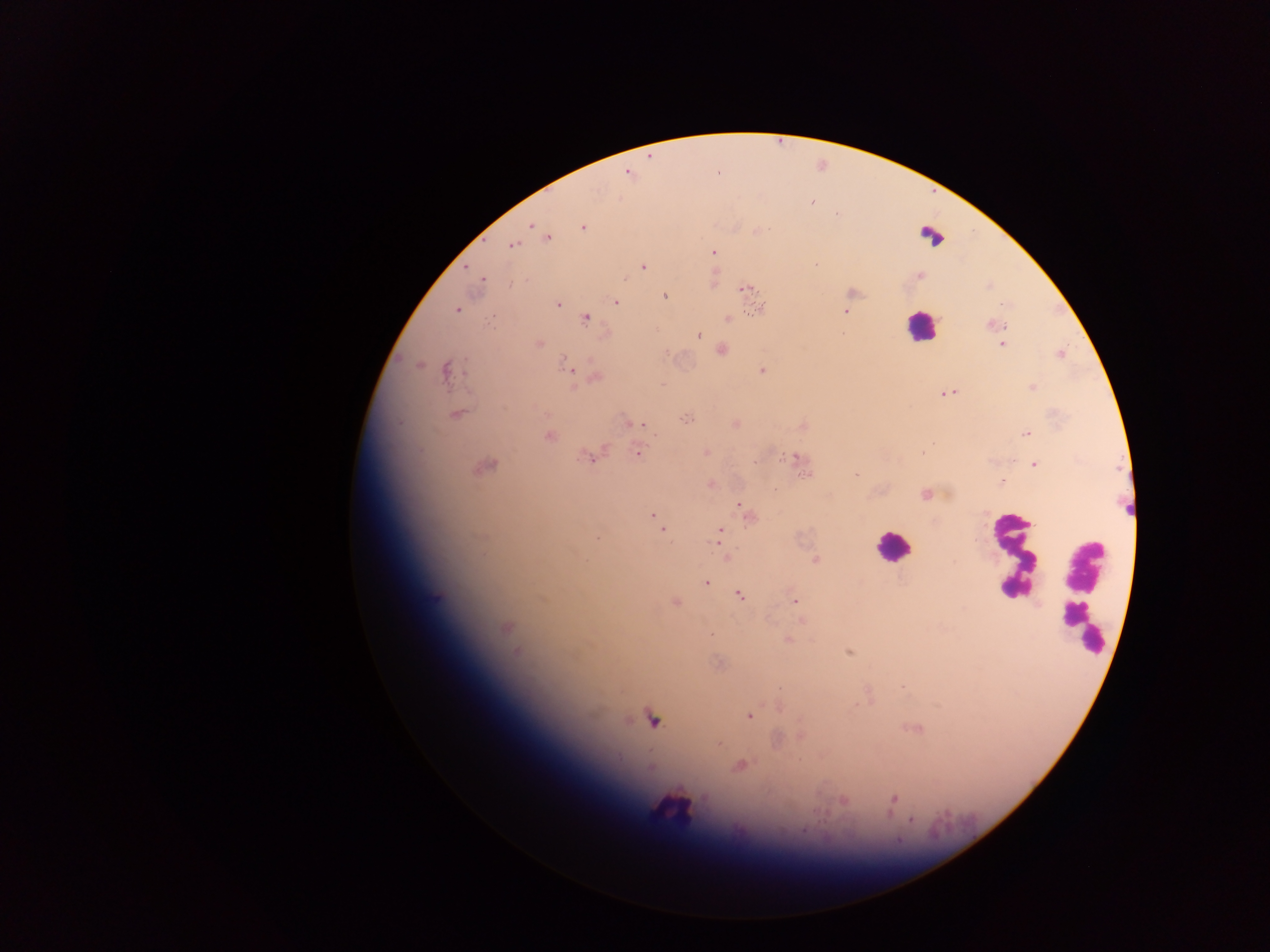
Approximate centers as x y in pixels.
Summary:
  - Leukocyte locations: 932 234; 920 327; 891 547; 1011 553; 1082 593; 674 806
  - Plasmodium parasite locations: 628 173; 811 203; 531 225; 583 227; 761 230; 547 238; 511 245; 713 253; 816 265; 643 267; 481 279; 745 288; 665 296; 616 302; 558 303; 1003 305; 760 308; 457 310; 844 311; 586 319; 727 319; 994 324; 698 336; 539 343; 1002 344; 721 351; 419 364; 567 366; 445 370; 762 371; 596 378; 947 393; 457 414; 684 419; 632 423; 1026 434; 549 436; 706 452; 638 453; 922 453; 587 457; 798 457; 1034 465; 486 466; 806 474; 855 475; 1001 483; 710 484; 925 494; 740 506; 652 516; 748 517; 657 521; 663 531; 719 534; 597 538; 718 543; 814 560; 706 582; 738 594; 795 602; 675 603; 802 619; 507 627; 712 634; 789 640; 516 652; 848 652; 719 664; 902 688; 749 716; 653 720; 720 744; 740 766; 893 799; 844 801; 912 819; 804 830
  - Preparation: thick blood smear
  - Capture: mobile-phone photograph through a microscope
  - Field of view: single
  - Country: Ghana
  - Image size: 1270×952 pixels